Describe the morphology of the red blood cells.
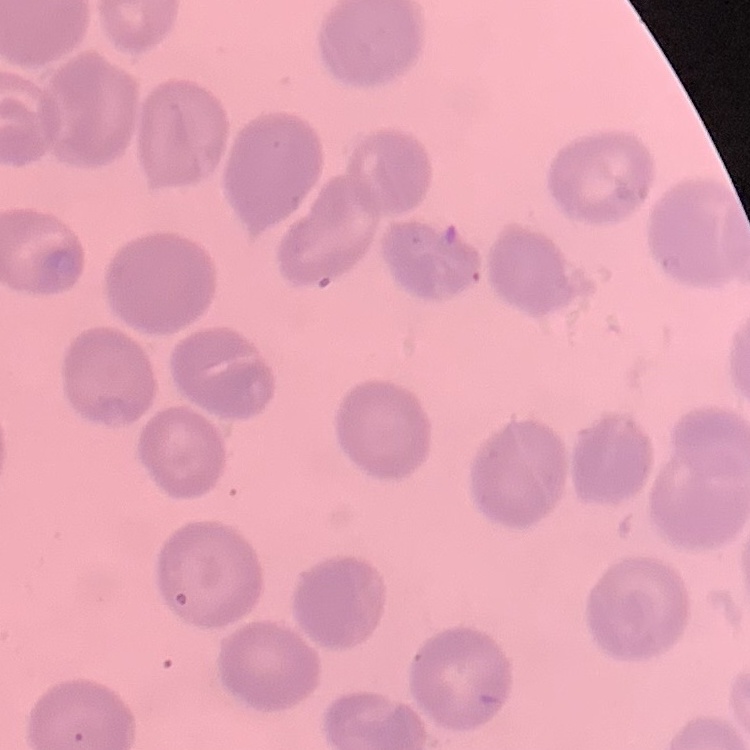
No rouleaux formation.

stain = Field's or Giemsa
image type = square crop of a larger photomicrograph
preparation = thin blood smear